Locate every blood parasite and identify its species.
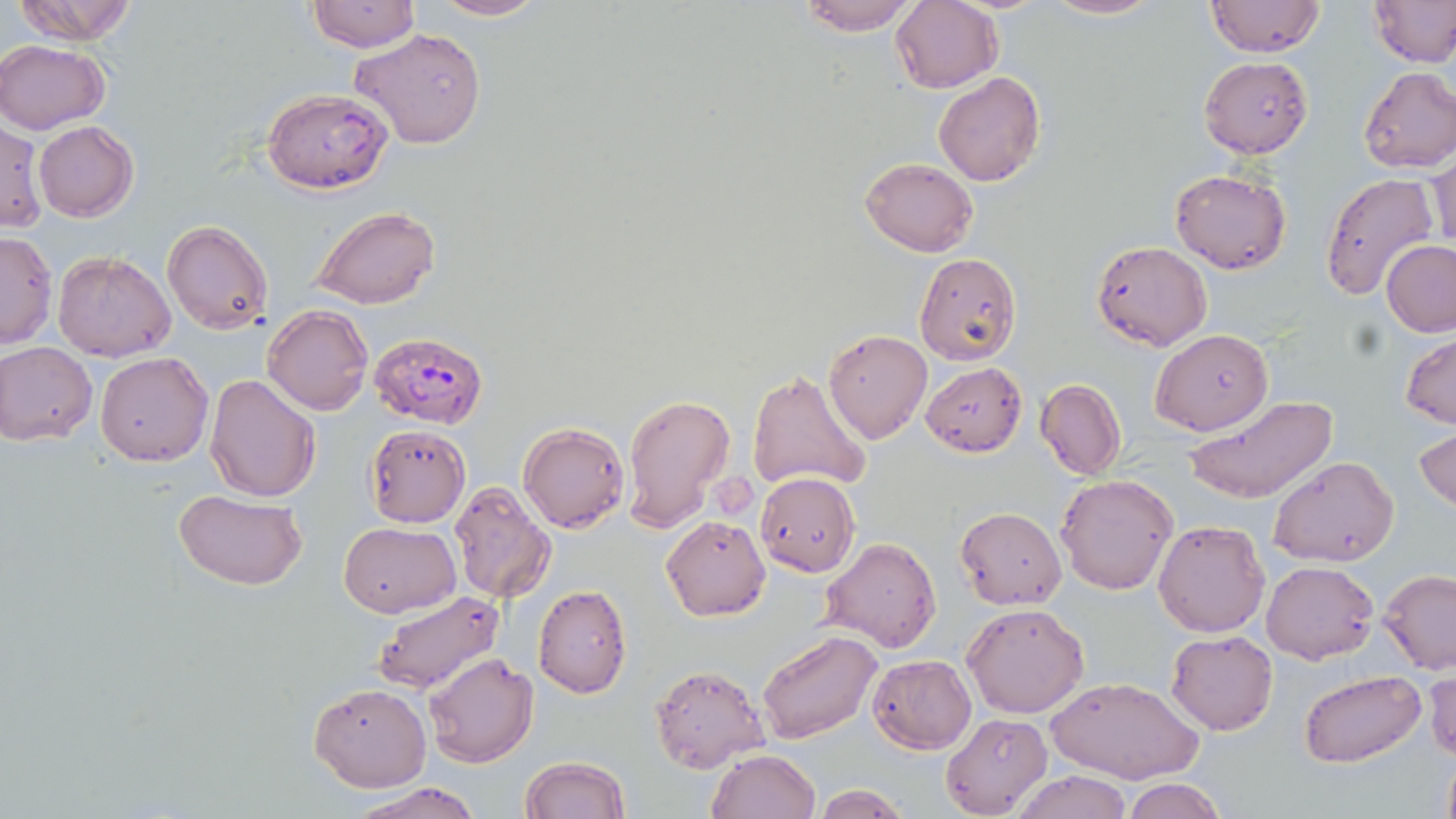
Approximate bounding boxes as named x1/y1/x2/y2 corners in pixels.
Plasmodium falciparum-infected red blood cells: (x1=370, y1=329, x2=487, y2=429).
No Plasmodium ovale, Plasmodium malariae, Plasmodium vivax, Babesia divergens, or Trypanosoma brucei observed.

slide-level diagnosis = Plasmodium falciparum
modality = optical microscopy
uninfected red blood cell locations = approximate bounding boxes as named x1/y1/x2/y2 corners in pixels: (x1=13, y1=0, x2=138, y2=45), (x1=426, y1=0, x2=550, y2=22), (x1=795, y1=0, x2=922, y2=35), (x1=1041, y1=0, x2=1163, y2=22), (x1=1204, y1=0, x2=1326, y2=59), (x1=1368, y1=0, x2=1456, y2=67), (x1=306, y1=1, x2=419, y2=52), (x1=890, y1=1, x2=1003, y2=92), (x1=351, y1=27, x2=487, y2=148), (x1=0, y1=39, x2=109, y2=134), (x1=1199, y1=55, x2=1313, y2=159), (x1=1358, y1=66, x2=1456, y2=173), (x1=933, y1=71, x2=1045, y2=187), (x1=261, y1=88, x2=393, y2=194), (x1=0, y1=119, x2=46, y2=234), (x1=33, y1=121, x2=139, y2=222), (x1=1428, y1=146, x2=1455, y2=256), (x1=859, y1=157, x2=978, y2=256), (x1=1169, y1=169, x2=1291, y2=275), (x1=1320, y1=173, x2=1438, y2=300), (x1=311, y1=207, x2=441, y2=310), (x1=161, y1=219, x2=272, y2=336), (x1=0, y1=229, x2=57, y2=349), (x1=1382, y1=239, x2=1456, y2=337), (x1=1092, y1=240, x2=1213, y2=351), (x1=53, y1=250, x2=177, y2=362), (x1=914, y1=252, x2=1021, y2=366), (x1=262, y1=304, x2=374, y2=416), (x1=1150, y1=327, x2=1271, y2=437), (x1=823, y1=328, x2=932, y2=444), (x1=1401, y1=331, x2=1455, y2=430), (x1=0, y1=340, x2=97, y2=446), (x1=94, y1=351, x2=213, y2=466), (x1=920, y1=362, x2=1027, y2=456), (x1=747, y1=368, x2=872, y2=496), (x1=204, y1=373, x2=321, y2=502), (x1=1035, y1=378, x2=1125, y2=480), (x1=622, y1=392, x2=737, y2=531), (x1=1185, y1=394, x2=1338, y2=505), (x1=519, y1=422, x2=629, y2=533), (x1=366, y1=424, x2=469, y2=527), (x1=1414, y1=424, x2=1456, y2=516), (x1=473, y1=449, x2=585, y2=586), (x1=1269, y1=456, x2=1398, y2=568), (x1=755, y1=472, x2=860, y2=576), (x1=1055, y1=474, x2=1178, y2=594), (x1=449, y1=479, x2=556, y2=602), (x1=173, y1=489, x2=307, y2=590), (x1=955, y1=507, x2=1067, y2=609), (x1=661, y1=516, x2=770, y2=621), (x1=1152, y1=520, x2=1270, y2=637), (x1=337, y1=521, x2=461, y2=618), (x1=821, y1=537, x2=943, y2=655), (x1=1262, y1=561, x2=1378, y2=663), (x1=1379, y1=569, x2=1456, y2=674), (x1=532, y1=584, x2=633, y2=697), (x1=370, y1=590, x2=505, y2=694), (x1=962, y1=602, x2=1090, y2=718), (x1=757, y1=629, x2=882, y2=745), (x1=1166, y1=631, x2=1278, y2=736), (x1=423, y1=651, x2=539, y2=768), (x1=868, y1=655, x2=975, y2=753), (x1=650, y1=664, x2=769, y2=772), (x1=1425, y1=664, x2=1456, y2=764), (x1=1298, y1=669, x2=1426, y2=768), (x1=1045, y1=675, x2=1202, y2=786), (x1=308, y1=683, x2=432, y2=792), (x1=940, y1=713, x2=1052, y2=817), (x1=705, y1=750, x2=819, y2=819), (x1=1438, y1=750, x2=1456, y2=819), (x1=520, y1=756, x2=632, y2=818), (x1=1013, y1=770, x2=1135, y2=819), (x1=1119, y1=778, x2=1231, y2=819), (x1=348, y1=781, x2=483, y2=819), (x1=810, y1=782, x2=912, y2=818)
field of view = single
image size = 1456×819 pixels
stain = May-Grünwald-Giemsa
preparation = thin blood smear
magnification = 1000x